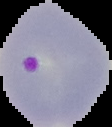
Summary:
  - Result: malaria parasites detected
  - Image size: 112×127 pixels
  - Image type: segmented cell region on a black background
  - Preparation: thin blood smear